Outline each Babesia divergens-infected red blood cell.
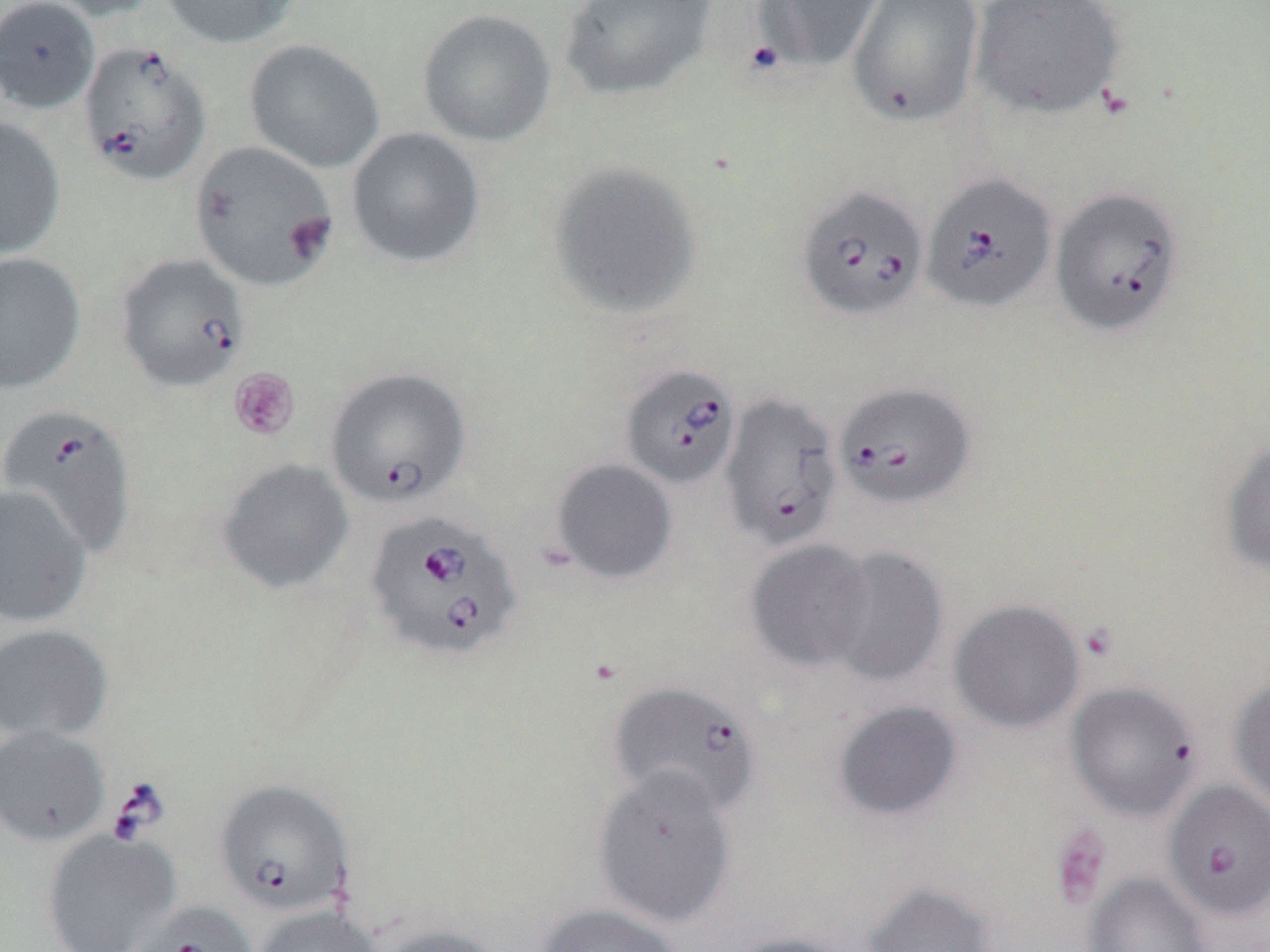

Approximate bounding boxes as [x1, y1, x2, y2] in pixels.
Babesia divergens-infected red blood cells: [78, 39, 212, 186], [921, 172, 1058, 314], [795, 184, 929, 322], [1050, 185, 1185, 338], [114, 252, 251, 392], [620, 363, 742, 490], [326, 368, 471, 509], [833, 382, 976, 511], [718, 389, 843, 551], [0, 402, 138, 556], [364, 510, 521, 663], [608, 680, 763, 819], [1065, 681, 1202, 821], [215, 778, 353, 917], [1164, 779, 1270, 921], [124, 900, 259, 952].

slide-level diagnosis = Babesia divergens
stain = May-Grünwald-Giemsa
magnification = 1000x
modality = optical microscopy
field of view = single
uninfected red blood cell locations = approximate bounding boxes as [x1, y1, x2, y2] in pixels: [0, 0, 100, 115], [37, 0, 166, 21], [158, 0, 302, 49], [559, 0, 718, 102], [753, 0, 887, 72], [847, 0, 984, 128], [970, 0, 1127, 120], [416, 8, 556, 148], [244, 39, 386, 173], [0, 115, 67, 260], [346, 127, 486, 268], [189, 140, 337, 292], [547, 159, 703, 320], [0, 252, 85, 395], [1222, 440, 1270, 574], [216, 458, 355, 595], [549, 458, 678, 585], [0, 485, 92, 629], [745, 539, 876, 672], [827, 545, 950, 687], [948, 599, 1085, 734], [0, 624, 114, 744], [1228, 676, 1270, 813], [831, 700, 964, 822], [0, 725, 110, 847], [592, 767, 737, 928], [42, 829, 181, 952], [1082, 871, 1212, 952], [856, 881, 1004, 952], [535, 903, 684, 952], [252, 904, 384, 952], [374, 923, 506, 952], [724, 932, 856, 952]
platelet locations = approximate bounding boxes as [x1, y1, x2, y2] in pixels: [228, 367, 300, 441], [1048, 824, 1112, 910]
preparation = thin blood smear
image size = 1270×952 pixels